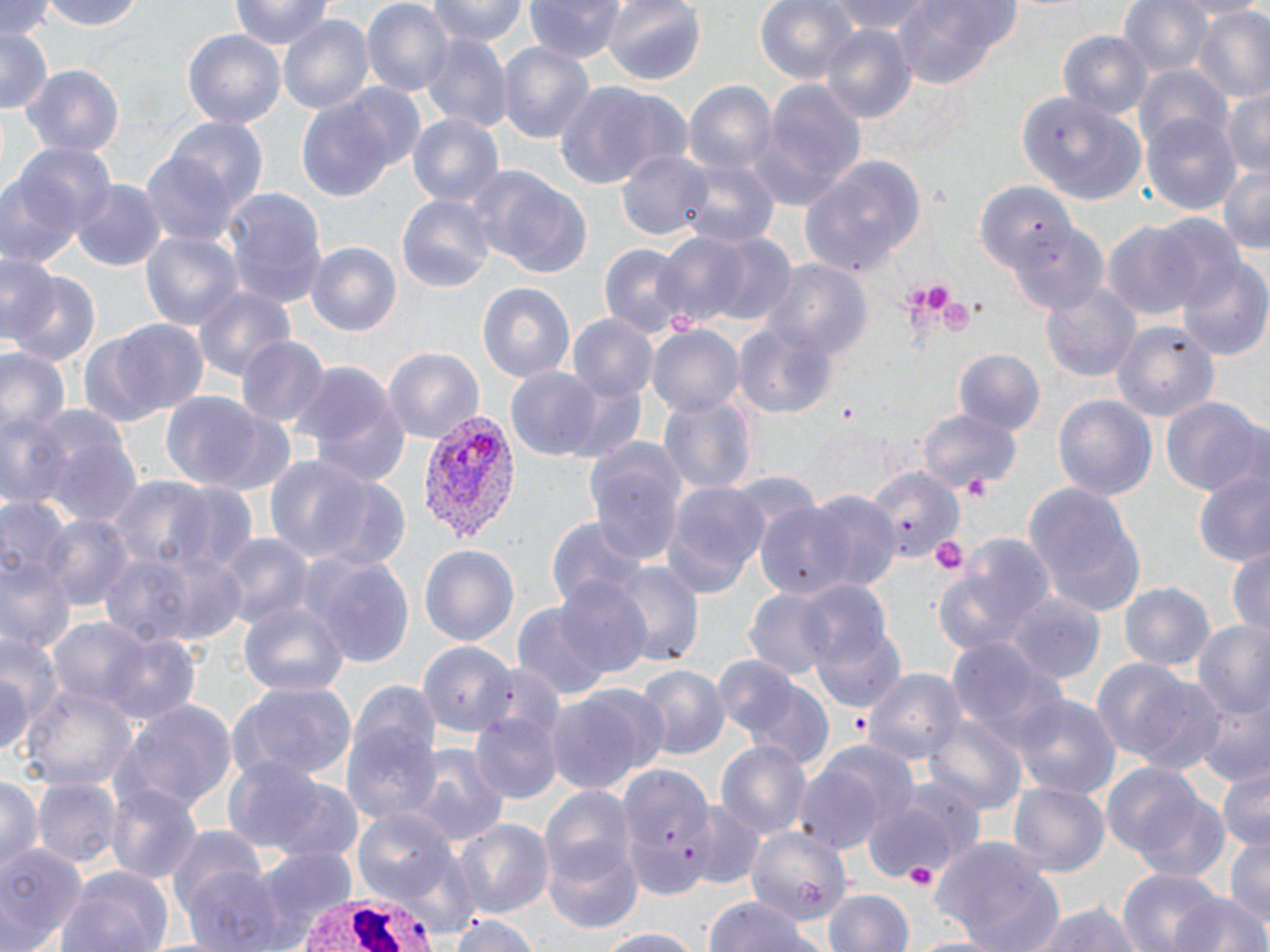
Summary:
  - Coordinate format: approximate bounding boxes as named x1/y1/x2/y2 corners in pixels
  - White blood cell locations: (x1=291, y1=893, x2=439, y2=952)
  - Plasmodium vivax-infected red blood cell locations: (x1=421, y1=409, x2=519, y2=543)
  - Uninfected red blood cell locations: (x1=2, y1=0, x2=58, y2=44), (x1=41, y1=0, x2=147, y2=33), (x1=232, y1=0, x2=332, y2=52), (x1=360, y1=0, x2=452, y2=96), (x1=423, y1=0, x2=530, y2=47), (x1=525, y1=0, x2=628, y2=64), (x1=602, y1=0, x2=707, y2=85), (x1=755, y1=0, x2=860, y2=84), (x1=830, y1=0, x2=936, y2=36), (x1=1119, y1=0, x2=1215, y2=80), (x1=889, y1=1, x2=1019, y2=88), (x1=1192, y1=8, x2=1270, y2=104), (x1=277, y1=13, x2=373, y2=113), (x1=819, y1=24, x2=917, y2=126), (x1=0, y1=28, x2=53, y2=113), (x1=1057, y1=30, x2=1155, y2=124), (x1=418, y1=31, x2=510, y2=132), (x1=182, y1=32, x2=284, y2=127), (x1=497, y1=40, x2=595, y2=148), (x1=1134, y1=64, x2=1231, y2=155), (x1=24, y1=66, x2=123, y2=156), (x1=683, y1=76, x2=778, y2=184), (x1=551, y1=79, x2=686, y2=189), (x1=749, y1=84, x2=866, y2=210), (x1=1221, y1=87, x2=1270, y2=177), (x1=293, y1=92, x2=407, y2=204), (x1=1020, y1=93, x2=1148, y2=205), (x1=406, y1=113, x2=503, y2=210), (x1=1144, y1=113, x2=1242, y2=214), (x1=166, y1=118, x2=268, y2=218), (x1=3, y1=147, x2=112, y2=267), (x1=617, y1=147, x2=713, y2=243), (x1=141, y1=151, x2=238, y2=250), (x1=799, y1=156, x2=927, y2=277), (x1=685, y1=159, x2=779, y2=249), (x1=1215, y1=161, x2=1270, y2=253), (x1=469, y1=171, x2=592, y2=278), (x1=70, y1=181, x2=165, y2=272), (x1=975, y1=182, x2=1075, y2=273), (x1=223, y1=189, x2=327, y2=313), (x1=395, y1=193, x2=495, y2=293), (x1=1151, y1=217, x2=1247, y2=314), (x1=1103, y1=221, x2=1203, y2=321), (x1=653, y1=226, x2=792, y2=330), (x1=139, y1=228, x2=243, y2=334), (x1=304, y1=240, x2=402, y2=335), (x1=597, y1=241, x2=694, y2=339), (x1=0, y1=252, x2=60, y2=344), (x1=1176, y1=256, x2=1270, y2=359), (x1=762, y1=261, x2=874, y2=365), (x1=4, y1=264, x2=100, y2=368), (x1=1039, y1=279, x2=1140, y2=384), (x1=193, y1=281, x2=294, y2=382), (x1=478, y1=282, x2=575, y2=384), (x1=567, y1=315, x2=658, y2=406), (x1=97, y1=319, x2=211, y2=424), (x1=733, y1=319, x2=838, y2=418), (x1=1113, y1=321, x2=1220, y2=421), (x1=646, y1=325, x2=744, y2=418), (x1=235, y1=333, x2=330, y2=428), (x1=0, y1=343, x2=69, y2=439), (x1=384, y1=348, x2=483, y2=444), (x1=954, y1=350, x2=1046, y2=436), (x1=292, y1=357, x2=407, y2=487), (x1=503, y1=368, x2=612, y2=459), (x1=551, y1=373, x2=650, y2=463), (x1=656, y1=390, x2=759, y2=497), (x1=161, y1=393, x2=267, y2=490), (x1=1052, y1=393, x2=1157, y2=500), (x1=1161, y1=396, x2=1264, y2=499), (x1=0, y1=406, x2=68, y2=510), (x1=24, y1=407, x2=141, y2=523), (x1=195, y1=407, x2=301, y2=497), (x1=918, y1=407, x2=1023, y2=493), (x1=581, y1=434, x2=689, y2=564), (x1=261, y1=452, x2=388, y2=569), (x1=866, y1=466, x2=961, y2=563), (x1=1192, y1=468, x2=1270, y2=569), (x1=309, y1=479, x2=412, y2=575), (x1=660, y1=479, x2=773, y2=599), (x1=1023, y1=484, x2=1146, y2=618), (x1=761, y1=489, x2=901, y2=599), (x1=2, y1=495, x2=75, y2=606), (x1=38, y1=512, x2=135, y2=612), (x1=546, y1=518, x2=647, y2=613), (x1=938, y1=533, x2=1057, y2=658), (x1=217, y1=535, x2=311, y2=634), (x1=99, y1=537, x2=250, y2=647), (x1=418, y1=543, x2=519, y2=650), (x1=1226, y1=543, x2=1270, y2=635), (x1=304, y1=554, x2=416, y2=671), (x1=1, y1=556, x2=72, y2=657), (x1=611, y1=563, x2=704, y2=667), (x1=552, y1=578, x2=654, y2=681), (x1=797, y1=581, x2=893, y2=678), (x1=1120, y1=581, x2=1213, y2=675), (x1=743, y1=587, x2=840, y2=679), (x1=1009, y1=594, x2=1105, y2=686), (x1=237, y1=596, x2=348, y2=704), (x1=808, y1=615, x2=906, y2=714), (x1=49, y1=617, x2=156, y2=711), (x1=1192, y1=620, x2=1270, y2=727), (x1=99, y1=631, x2=204, y2=730), (x1=947, y1=638, x2=1072, y2=756), (x1=418, y1=639, x2=517, y2=741), (x1=0, y1=645, x2=39, y2=761), (x1=711, y1=655, x2=804, y2=749), (x1=1093, y1=658, x2=1227, y2=774), (x1=635, y1=666, x2=729, y2=760), (x1=865, y1=668, x2=963, y2=768), (x1=737, y1=676, x2=839, y2=772), (x1=228, y1=679, x2=359, y2=784), (x1=18, y1=684, x2=136, y2=793), (x1=545, y1=688, x2=660, y2=796), (x1=1011, y1=693, x2=1121, y2=801), (x1=1194, y1=700, x2=1270, y2=787), (x1=117, y1=701, x2=237, y2=812), (x1=474, y1=711, x2=559, y2=802), (x1=340, y1=713, x2=445, y2=833), (x1=926, y1=716, x2=1025, y2=814), (x1=717, y1=738, x2=811, y2=842), (x1=815, y1=741, x2=920, y2=838), (x1=409, y1=744, x2=508, y2=849), (x1=221, y1=756, x2=335, y2=857), (x1=792, y1=765, x2=881, y2=855), (x1=1215, y1=765, x2=1270, y2=849), (x1=1110, y1=772, x2=1229, y2=881), (x1=0, y1=773, x2=43, y2=875), (x1=253, y1=773, x2=370, y2=867), (x1=33, y1=777, x2=120, y2=866), (x1=1008, y1=781, x2=1109, y2=877), (x1=106, y1=783, x2=203, y2=887), (x1=863, y1=784, x2=977, y2=882), (x1=541, y1=785, x2=639, y2=896), (x1=691, y1=801, x2=764, y2=887), (x1=353, y1=807, x2=463, y2=906), (x1=452, y1=818, x2=554, y2=923), (x1=167, y1=821, x2=272, y2=933), (x1=745, y1=826, x2=850, y2=924), (x1=1224, y1=836, x2=1270, y2=931), (x1=932, y1=840, x2=1067, y2=952), (x1=0, y1=841, x2=86, y2=952), (x1=545, y1=841, x2=643, y2=935), (x1=243, y1=846, x2=358, y2=946), (x1=177, y1=863, x2=294, y2=952), (x1=57, y1=867, x2=174, y2=952), (x1=1116, y1=868, x2=1226, y2=952), (x1=824, y1=888, x2=915, y2=952), (x1=1170, y1=894, x2=1269, y2=952), (x1=702, y1=895, x2=819, y2=952), (x1=1028, y1=900, x2=1146, y2=952), (x1=450, y1=910, x2=540, y2=952), (x1=585, y1=926, x2=705, y2=950), (x1=905, y1=934, x2=1009, y2=952)
  - Platelet locations: (x1=925, y1=285, x2=950, y2=310), (x1=836, y1=405, x2=863, y2=427), (x1=958, y1=474, x2=996, y2=502), (x1=925, y1=534, x2=970, y2=579), (x1=846, y1=708, x2=872, y2=740), (x1=903, y1=859, x2=938, y2=889)
  - Slide-level diagnosis: Plasmodium vivax
  - Stain: May-Grünwald-Giemsa
  - Preparation: thin blood film
  - Magnification: 1000x
  - Image size: 1270×952 pixels
  - Modality: light microscopy
  - Field of view: one of a larger specimen